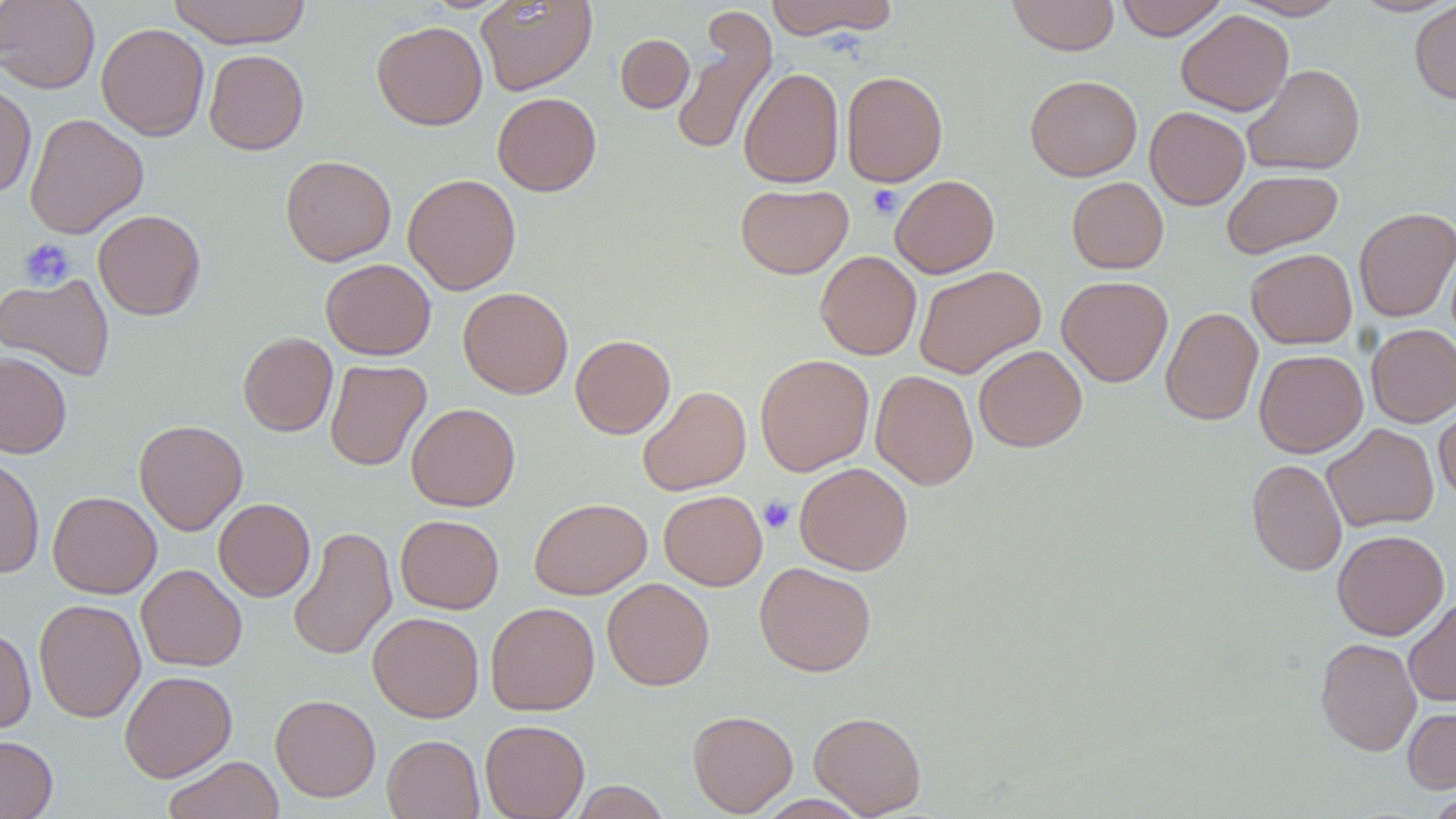

Approximate bounding boxes as (x1, y1, x2, y2) in pixels. Uninfected red blood cell locations: (0, 0, 100, 93), (167, 0, 312, 48), (475, 0, 597, 96), (765, 0, 899, 40), (1006, 0, 1120, 56), (1115, 0, 1227, 40), (1232, 0, 1349, 20), (1350, 0, 1456, 17), (1409, 1, 1456, 104), (1176, 10, 1294, 115), (671, 12, 776, 158), (372, 20, 488, 130), (96, 23, 210, 141), (615, 34, 695, 112), (204, 49, 309, 154), (1243, 64, 1365, 176), (739, 67, 844, 188), (841, 70, 948, 186), (1025, 75, 1142, 181), (0, 82, 36, 198), (492, 92, 601, 196), (1145, 106, 1249, 210), (24, 113, 148, 238), (280, 155, 396, 266), (1222, 169, 1343, 258), (403, 173, 521, 295), (890, 175, 999, 278), (1067, 177, 1168, 274), (735, 184, 853, 279), (1353, 207, 1456, 322), (93, 209, 206, 320), (1246, 248, 1357, 349), (816, 251, 921, 360), (320, 258, 435, 360), (914, 265, 1045, 379), (0, 273, 115, 381), (1057, 275, 1173, 387), (458, 286, 573, 399), (1161, 306, 1263, 425), (1366, 324, 1456, 427), (238, 332, 338, 436), (570, 334, 676, 438), (973, 345, 1087, 452), (1254, 350, 1367, 457), (0, 352, 72, 458), (755, 354, 874, 476), (325, 359, 431, 471), (871, 370, 978, 490), (637, 385, 751, 496), (1434, 400, 1456, 503), (406, 403, 520, 511), (134, 419, 247, 535), (1322, 423, 1439, 532), (0, 454, 45, 578), (1246, 459, 1347, 576), (794, 462, 913, 575), (659, 490, 767, 591), (47, 491, 161, 598), (214, 498, 315, 601), (529, 498, 652, 599), (395, 514, 504, 614), (288, 525, 397, 661), (1332, 529, 1449, 641), (754, 561, 876, 677), (136, 564, 247, 671), (602, 577, 714, 691), (1403, 596, 1456, 707), (33, 598, 145, 723), (486, 602, 599, 716), (368, 612, 484, 722), (0, 627, 36, 735), (1315, 637, 1422, 756), (120, 670, 237, 782), (270, 694, 381, 802), (1403, 705, 1456, 793), (687, 710, 798, 816), (809, 710, 927, 817), (480, 719, 589, 819), (0, 734, 58, 819), (382, 734, 484, 819), (163, 755, 284, 819), (568, 781, 672, 819), (1426, 791, 1456, 818). Platelet locations: (867, 184, 902, 219), (17, 238, 75, 290), (759, 495, 796, 534). Slide-level diagnosis: negative for blood parasites. Optical microscopy. One field of a larger specimen. 1000x magnification. Thin blood smear. May-Grünwald-Giemsa-stained preparation. Image is 1456×819 pixels.